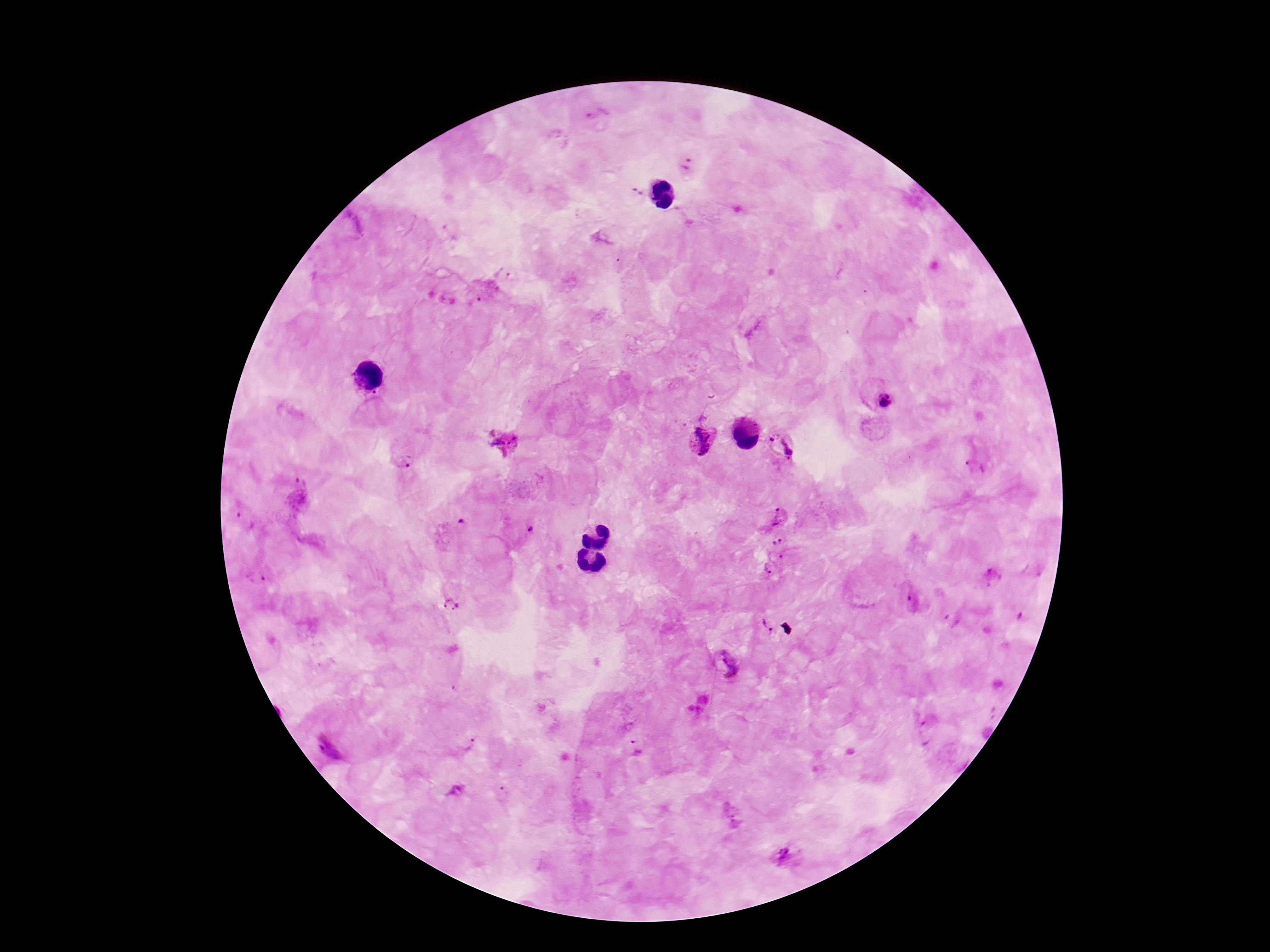 Approximate centers as [x, y] in pixels. Plasmodium parasite locations: [598, 115], [689, 165], [637, 193], [449, 231], [484, 292], [878, 395], [374, 398], [502, 439], [703, 440], [782, 446], [404, 463], [975, 468], [302, 478], [780, 517], [246, 521], [461, 521], [530, 528], [775, 553], [266, 574], [991, 578], [910, 601], [451, 604], [952, 620], [767, 628], [724, 664], [926, 732], [469, 741], [635, 747], [456, 790], [502, 797], [731, 816], [789, 856]. Giemsa stain. Single field of view. Smartphone photograph taken through the microscope eyepiece. Image is 1270×952 pixels. 100x magnification. Patient malaria status: positive. Thick blood smear.